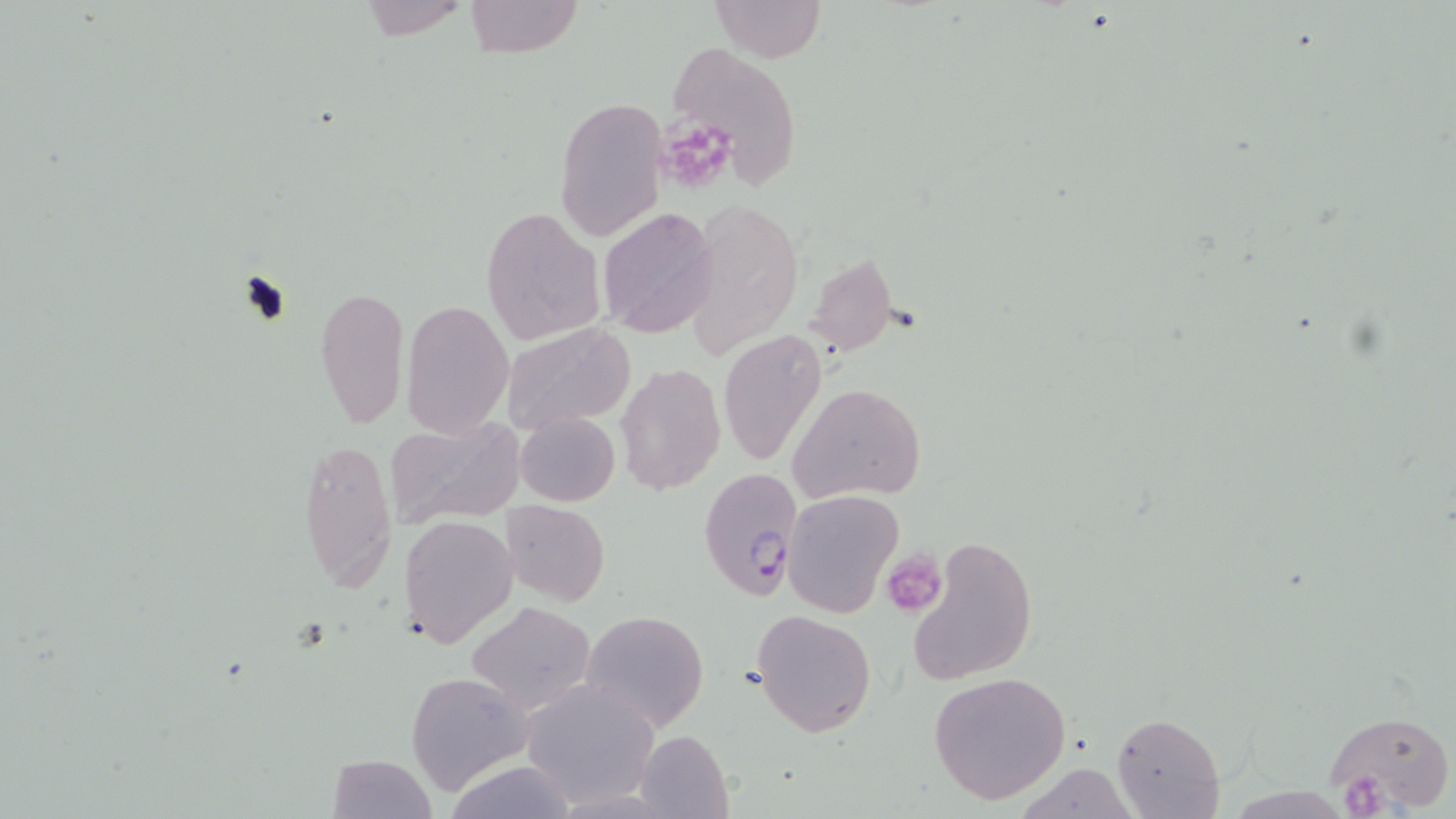

Summary:
  - Coordinate format: approximate bounding boxes as (x1, y1, x2, y2) in pixels
  - Uninfected red blood cell locations: (466, 0, 582, 58), (709, 0, 825, 64), (351, 2, 475, 39), (665, 41, 803, 188), (553, 96, 668, 241), (598, 206, 720, 340), (479, 207, 606, 345), (313, 283, 410, 430), (402, 299, 515, 438), (502, 322, 637, 433), (718, 329, 829, 468), (615, 363, 725, 496), (790, 382, 927, 503), (515, 412, 620, 508), (387, 417, 523, 530), (297, 435, 396, 592), (782, 489, 903, 617), (500, 499, 610, 605), (399, 515, 519, 650), (907, 533, 1037, 686), (466, 601, 596, 714), (751, 609, 876, 738), (581, 610, 708, 729), (405, 671, 533, 793), (928, 672, 1071, 805), (520, 679, 661, 808), (1323, 707, 1454, 814), (1112, 713, 1225, 819), (633, 730, 735, 819), (325, 753, 437, 819), (443, 760, 580, 819), (1010, 762, 1144, 819)
  - Platelet locations: (881, 549, 945, 615), (1342, 772, 1393, 818)
  - Plasmodium falciparum-infected red blood cell locations: (660, 118, 735, 190), (698, 466, 805, 603)
  - Slide-level diagnosis: Plasmodium falciparum
  - Preparation: thin blood smear
  - Field of view: one of a larger specimen
  - Magnification: 1000x
  - Modality: light microscopy
  - Stain: May-Grünwald-Giemsa
  - Image size: 1456×819 pixels